Give the preparation type.
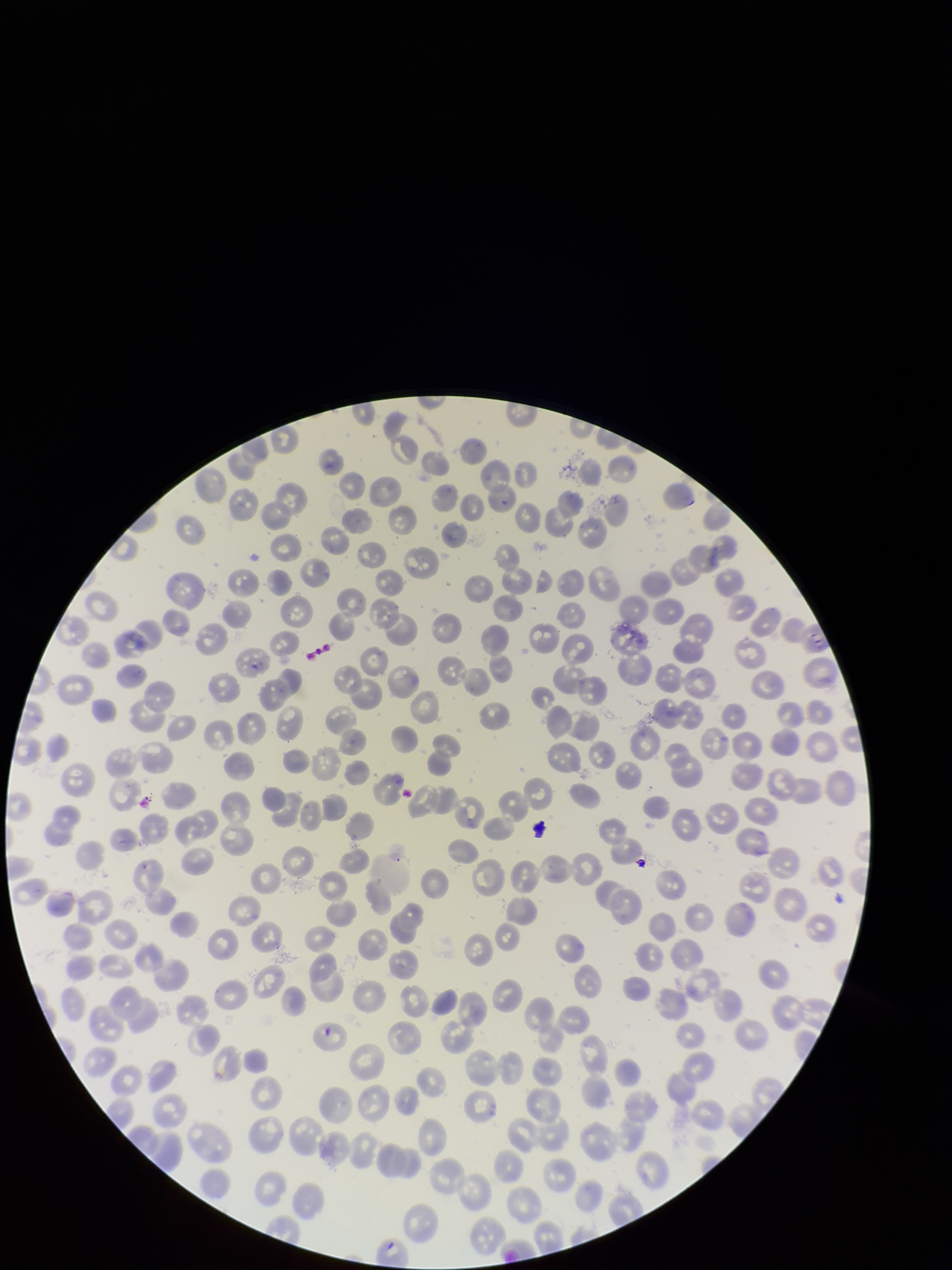
Thin.

Summary:
  - Image size: 952×1270 pixels
  - Red blood cell count: 248
  - Species reported for this patient: Plasmodium falciparum
  - Capture: smartphone photograph through the microscope eyepiece
  - Parasitized red blood cell count: 0
  - Field of view: one from this slide
  - Patient malaria status: infected
  - Stain: Giemsa
  - Parasitized red blood cells: none detected